Outline each blood parasite and name the species.
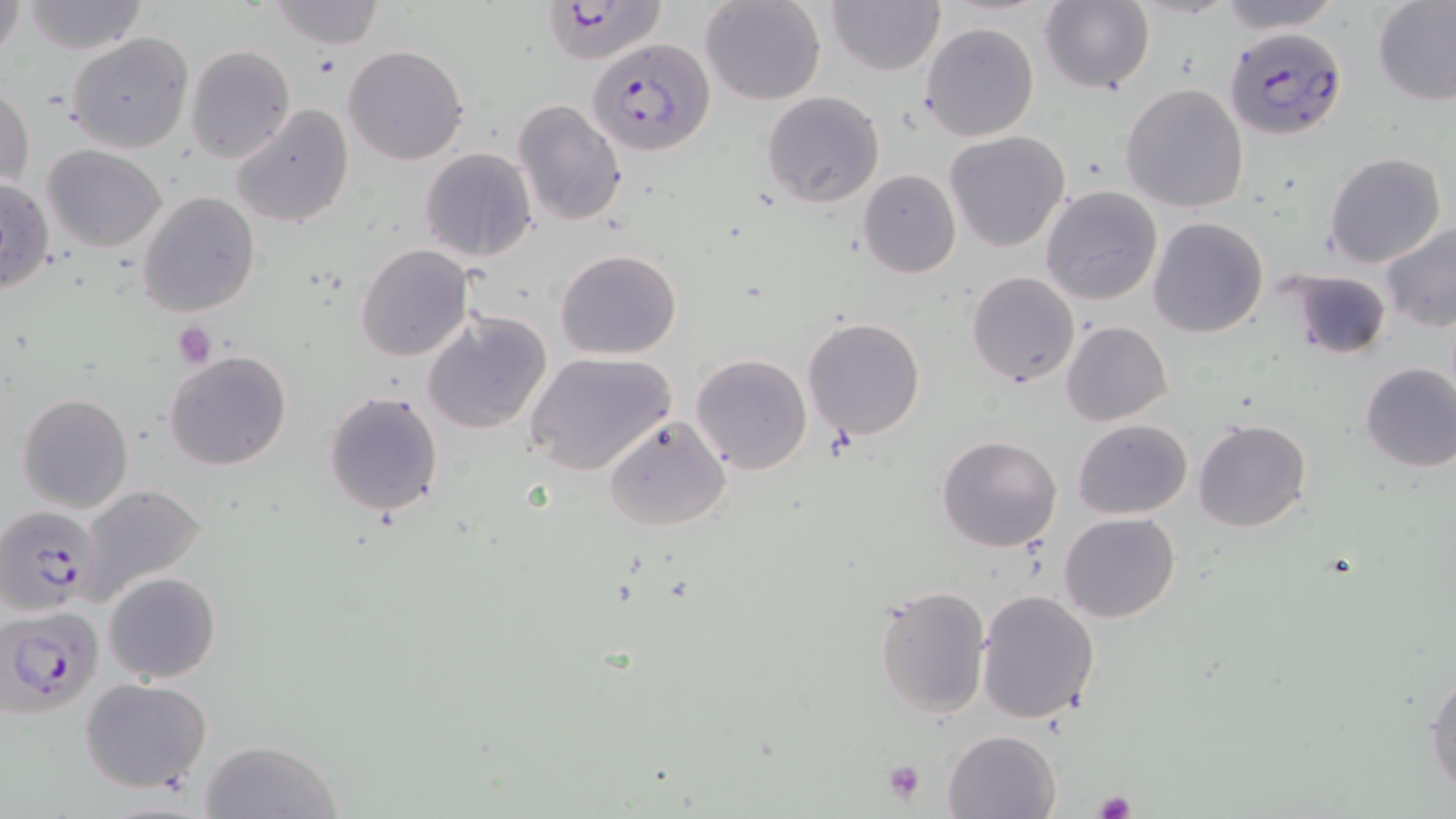
Approximate bounding boxes as named x1/y1/x2/y2 corners in pixels.
Plasmodium falciparum-infected red blood cells: (x1=540, y1=2, x2=665, y2=60), (x1=1223, y1=25, x2=1348, y2=140), (x1=586, y1=36, x2=713, y2=159), (x1=5, y1=493, x2=103, y2=604), (x1=2, y1=606, x2=104, y2=718).
No Plasmodium ovale, Plasmodium malariae, Plasmodium vivax, Babesia divergens, or Trypanosoma brucei observed.

Uninfected red blood cell locations: (x1=1, y1=0, x2=26, y2=69), (x1=21, y1=0, x2=149, y2=55), (x1=270, y1=0, x2=384, y2=48), (x1=700, y1=0, x2=827, y2=106), (x1=1215, y1=0, x2=1345, y2=33), (x1=1372, y1=0, x2=1456, y2=105), (x1=827, y1=1, x2=945, y2=76), (x1=1040, y1=1, x2=1155, y2=95), (x1=919, y1=22, x2=1040, y2=143), (x1=65, y1=32, x2=194, y2=155), (x1=186, y1=45, x2=296, y2=164), (x1=342, y1=45, x2=469, y2=166), (x1=0, y1=78, x2=34, y2=194), (x1=1121, y1=82, x2=1251, y2=214), (x1=760, y1=92, x2=885, y2=208), (x1=511, y1=98, x2=628, y2=230), (x1=229, y1=104, x2=353, y2=229), (x1=943, y1=130, x2=1070, y2=253), (x1=42, y1=146, x2=168, y2=252), (x1=419, y1=148, x2=539, y2=263), (x1=1323, y1=152, x2=1446, y2=268), (x1=857, y1=169, x2=961, y2=278), (x1=1, y1=176, x2=55, y2=295), (x1=1041, y1=186, x2=1162, y2=307), (x1=137, y1=191, x2=261, y2=318), (x1=1148, y1=218, x2=1269, y2=337), (x1=1380, y1=219, x2=1456, y2=331), (x1=355, y1=244, x2=473, y2=363), (x1=555, y1=248, x2=684, y2=359), (x1=1283, y1=268, x2=1390, y2=360), (x1=967, y1=271, x2=1079, y2=387), (x1=421, y1=308, x2=552, y2=434), (x1=803, y1=318, x2=926, y2=440), (x1=1062, y1=321, x2=1172, y2=425), (x1=164, y1=351, x2=293, y2=472), (x1=524, y1=352, x2=677, y2=476), (x1=691, y1=354, x2=812, y2=475), (x1=1358, y1=361, x2=1456, y2=472), (x1=322, y1=389, x2=447, y2=518), (x1=17, y1=391, x2=134, y2=514), (x1=603, y1=415, x2=732, y2=532), (x1=1072, y1=419, x2=1193, y2=520), (x1=1193, y1=419, x2=1311, y2=533), (x1=936, y1=435, x2=1062, y2=553), (x1=79, y1=483, x2=208, y2=601), (x1=1059, y1=512, x2=1180, y2=623), (x1=104, y1=572, x2=221, y2=682), (x1=873, y1=584, x2=992, y2=720), (x1=976, y1=589, x2=1101, y2=725), (x1=1426, y1=666, x2=1456, y2=799), (x1=80, y1=677, x2=212, y2=793), (x1=943, y1=728, x2=1061, y2=818), (x1=201, y1=740, x2=344, y2=819). Platelet locations: (x1=172, y1=322, x2=217, y2=368), (x1=881, y1=760, x2=927, y2=804), (x1=1093, y1=791, x2=1136, y2=818). Slide-level diagnosis: Plasmodium falciparum. Light microscopy. Single field of view. Image is 1456×819 pixels. Thin blood film. May-Grünwald-Giemsa-stained preparation. Captured at 1000x magnification.